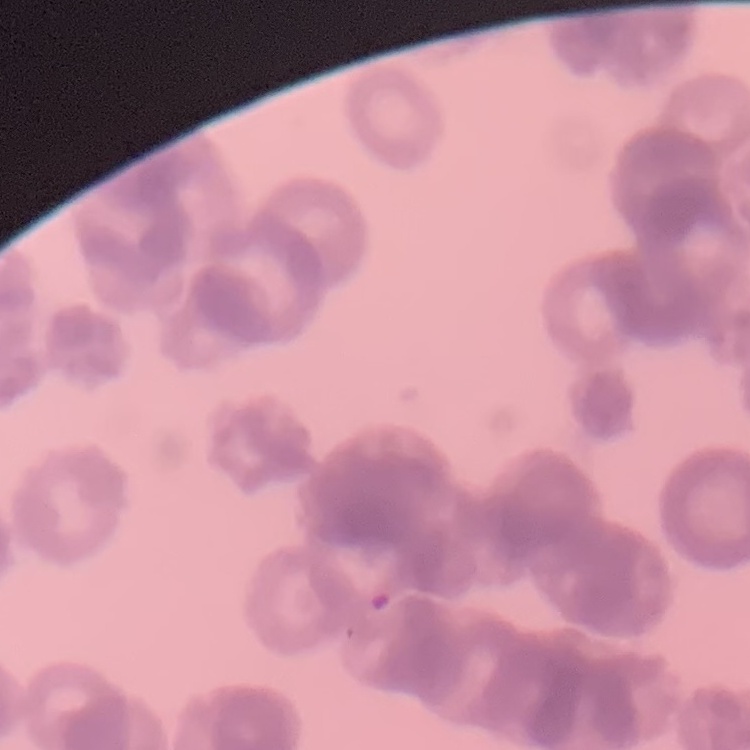
red_blood_cell_morphology: rouleaux formation
preparation: thin peripheral smear
stain: Field's or Giemsa
image_type: one tile cut from a larger photomicrograph